Locate every leukocyte (white blood cell).
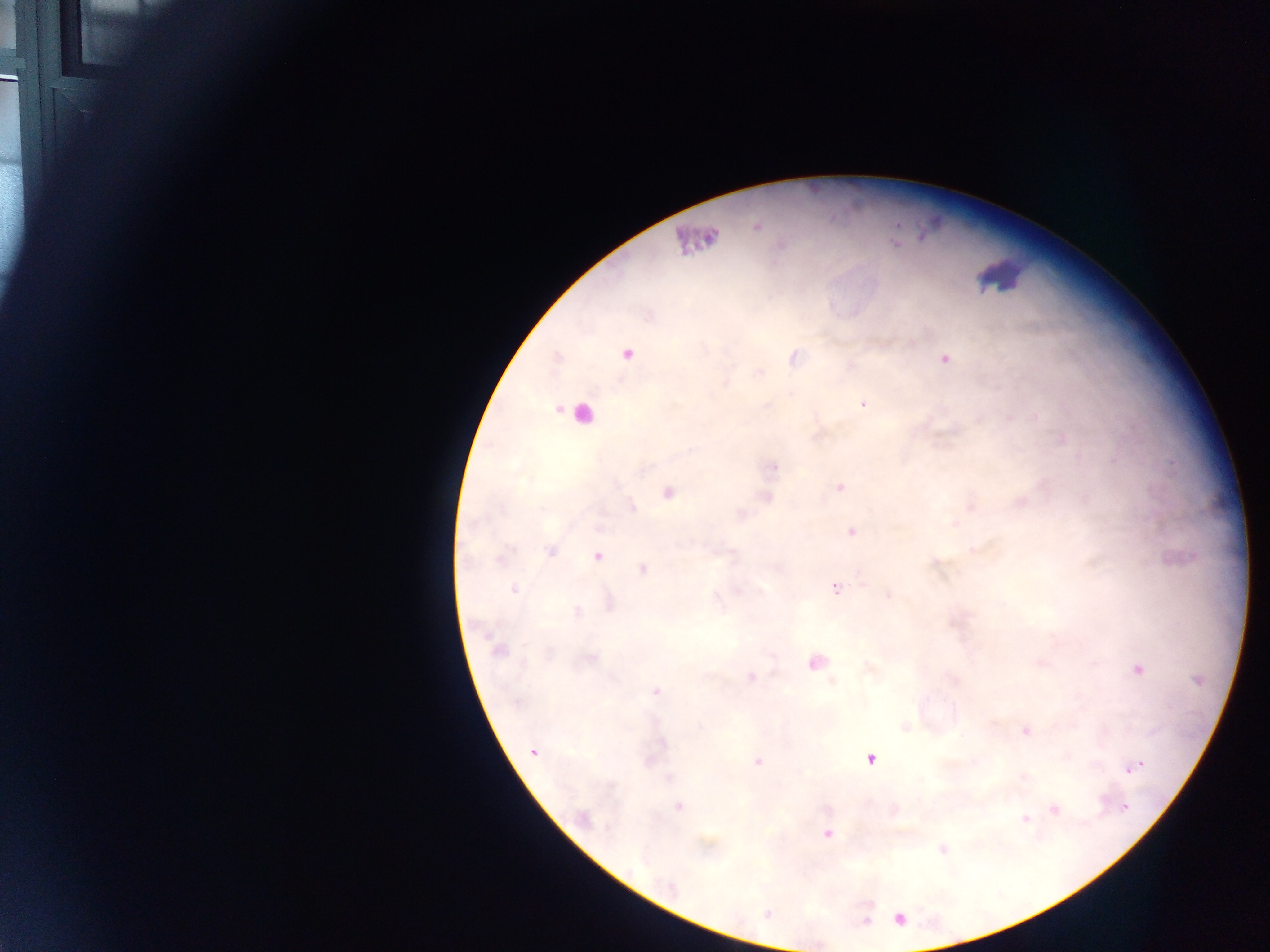

Approximate centers as x y in pixels.
Leukocytes: 1001 274; 578 414.

capture = mobile-phone photograph through a microscope
country = Ghana
field of view = single
image size = 1270×952 pixels
preparation = thick blood film
Plasmodium parasite locations = approximate centers as x y in pixels: 758 226; 627 355; 944 359; 863 405; 1113 461; 774 468; 839 487; 668 492; 633 507; 852 532; 551 550; 597 557; 642 569; 836 588; 514 589; 888 595; 577 611; 498 651; 1138 669; 751 677; 655 691; 1027 731; 533 752; 870 759; 758 762; 1136 767; 1130 770; 1024 777; 669 778; 679 807; 1124 807; 1054 810; 583 817; 1025 819; 827 834; 900 919